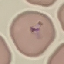

malaria status = parasitized
image type = cell patch, automatically extracted from a larger field of view and resized to 64 × 64 pixels
capture = smartphone camera at the microscope eyepiece
preparation = thin blood smear
stain = Giemsa